Assess this cell for malaria.
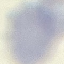
Uninfected.

Thin blood smear. Giemsa-stained preparation. Cell patch, automatically extracted from a larger field of view and resized to 64 × 64 pixels. Acquired by smartphone through the microscope eyepiece.